Describe the morphology of the erythrocytes.
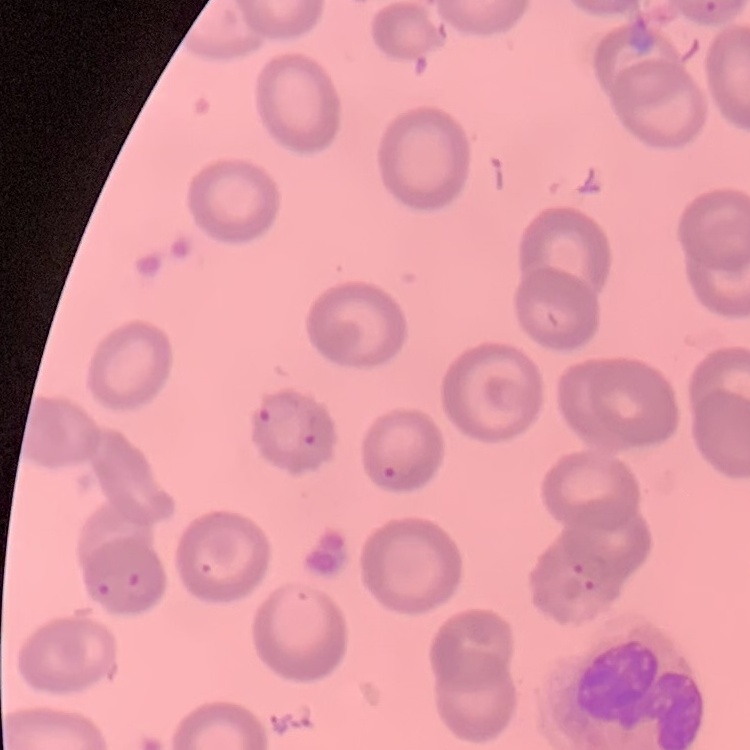
They show no rouleaux formation.

image_type: square crop of a larger photomicrograph
stain: Field's or Giemsa
preparation: thin blood smear